Locate every malaria parasite.
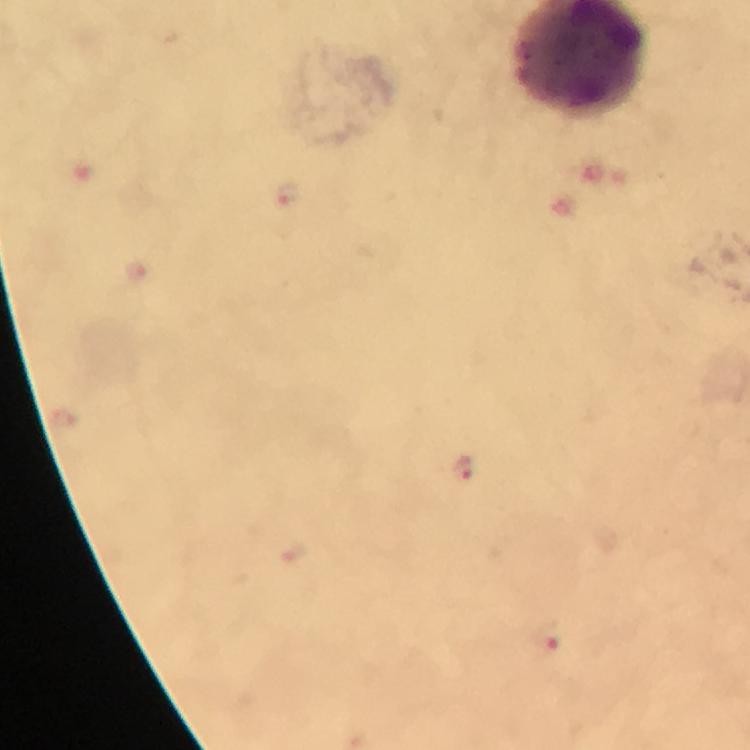
Approximate centers as (x, y) in pixels.
Malaria parasites: (287, 192), (463, 469), (546, 636).

Summary:
  - Capture: smartphone camera through the microscope
  - Cropped from: one field of view
  - Magnification: 100x
  - Context: from a malaria diagnostic workup
  - Preparation: thick smear
  - Stain: Giemsa
  - Image size: 750×750 pixels
  - Immersion oil: used